State the preparation type.
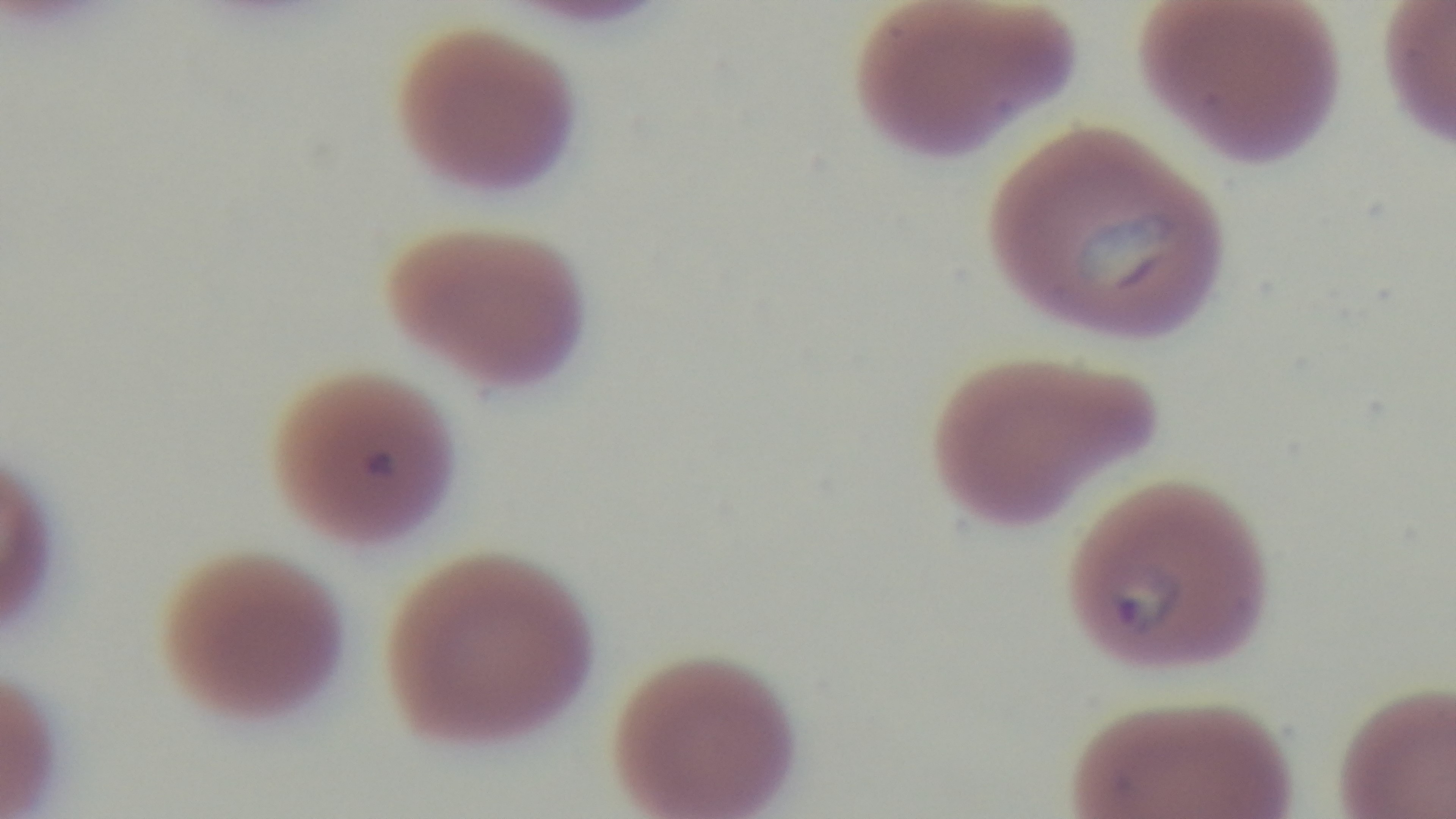

It is a thin blood film.

stain = Giemsa
modality = light microscopy
objective = 100x oil immersion
field of view = one from the slide
capture = mounted 4K digital camera
malaria status = infected